Point out each Plasmodium parasite.
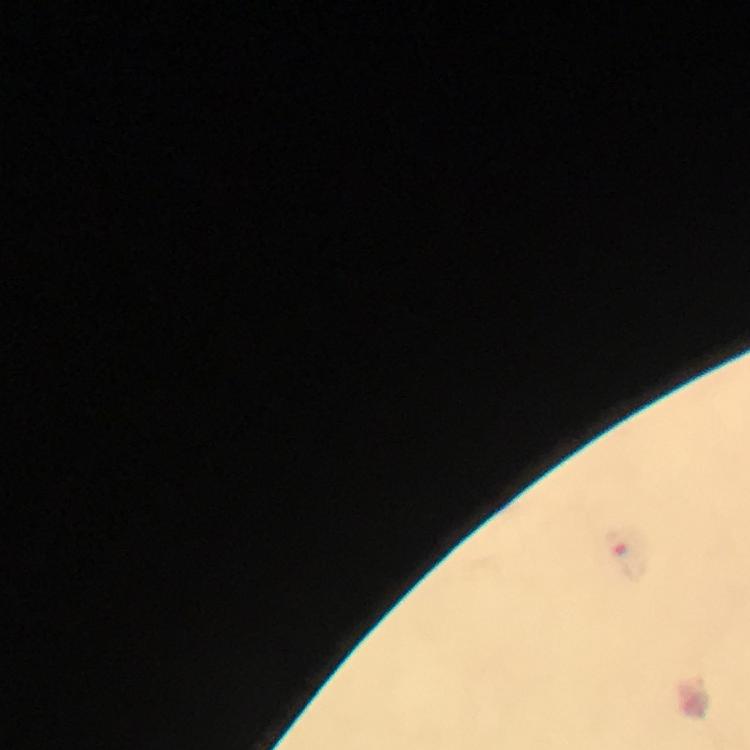
Approximate centers as (x, y) in pixels.
Plasmodium parasites: (630, 563).

stain = Giemsa
immersion oil = used
magnification = 100x
capture = smartphone photograph through a microscope
cropped from = a single field of view
context = from a malaria diagnostic workup
preparation = thick blood film
image size = 750×750 pixels